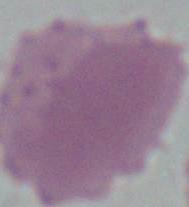
{
  "identification": "red blood cell",
  "modality": "micrograph",
  "magnification": "1000x"
}